Locate every malaria parasite.
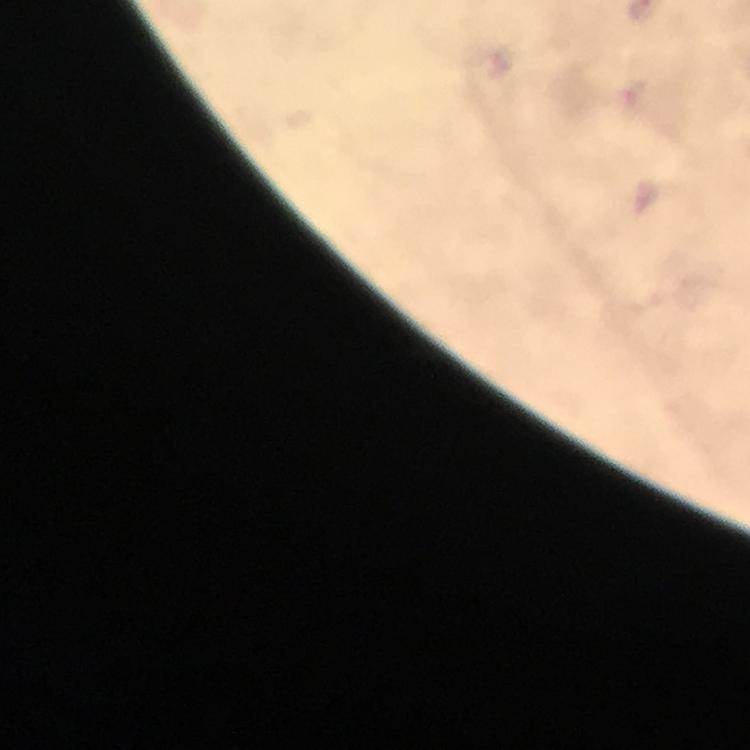

Approximate centers as (x, y) in pixels.
Malaria parasites: (633, 94).

stain: Giemsa
context: from a malaria diagnostic workup
image_size: 750×750 pixels
capture: smartphone mounted on the microscope
preparation: thick blood smear
cropped_from: a single field of view
magnification: 100x
immersion_oil: applied